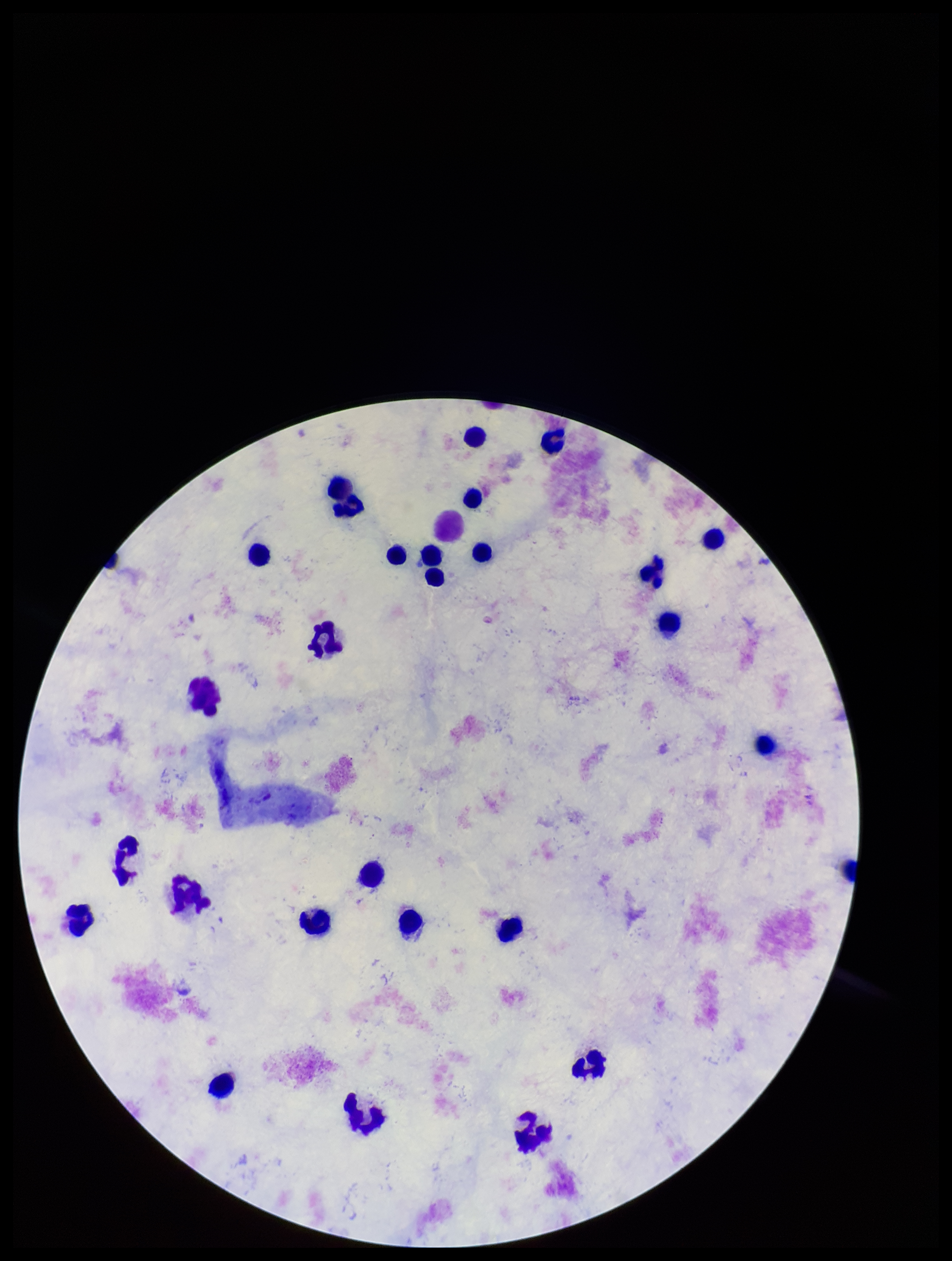

{
  "plasmodium_parasites": "none seen",
  "patient_malaria_status": "negative",
  "preparation": "thick smear",
  "leukocyte_count": 29,
  "field_of_view": "one from this slide",
  "image_size": "952×1261 pixels",
  "capture": "smartphone photograph through the microscope eyepiece",
  "parasite_count": 0,
  "stain": "Giemsa"
}